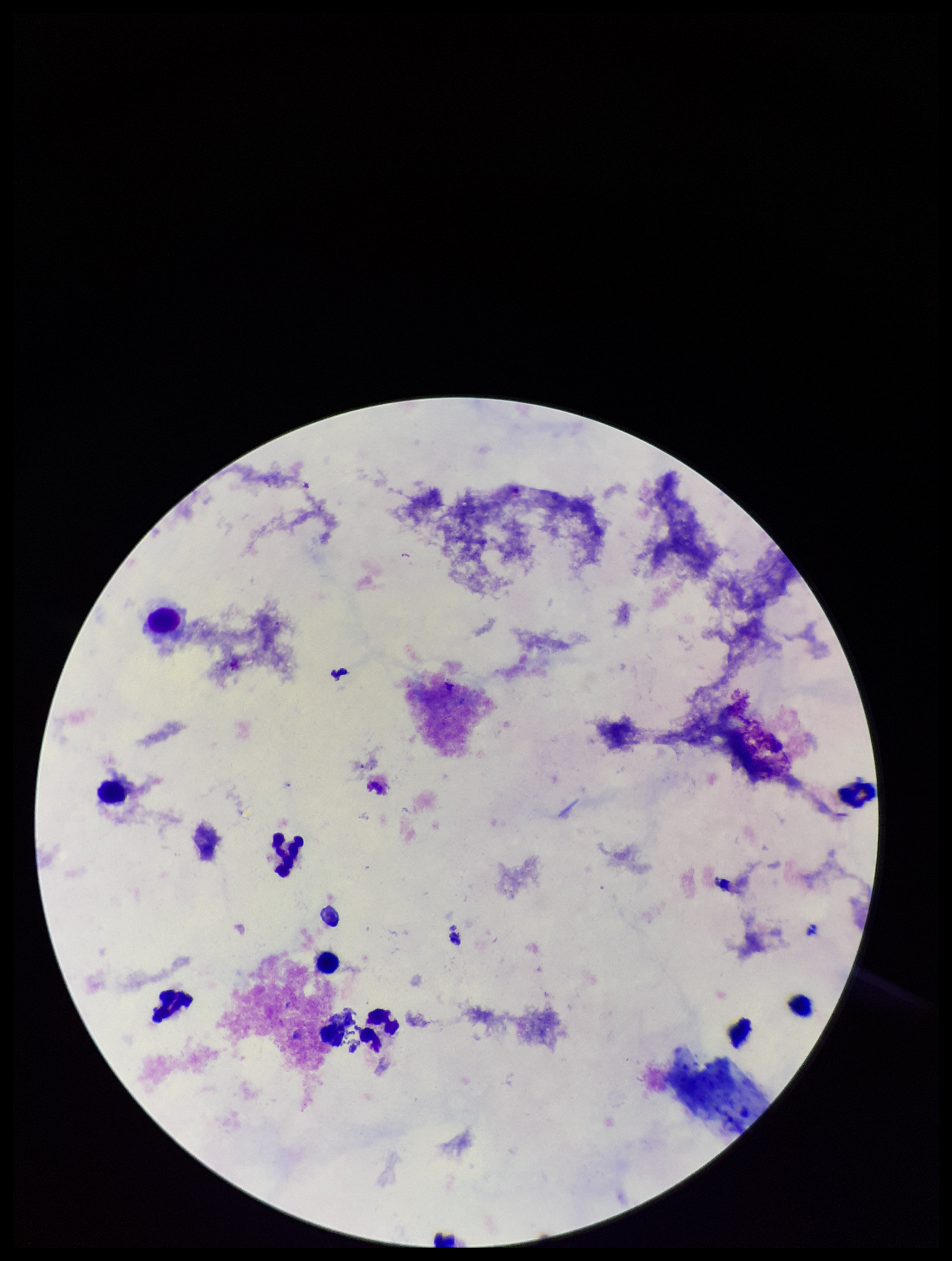
capture = smartphone photograph through the microscope eyepiece
leukocyte count = 10
stain = Giemsa
field of view = one from this slide
preparation = thick blood smear
parasite count = 0
image size = 952×1261 pixels
Plasmodium parasites = none seen
patient malaria status = negative